Describe the morphology of the red blood cells.
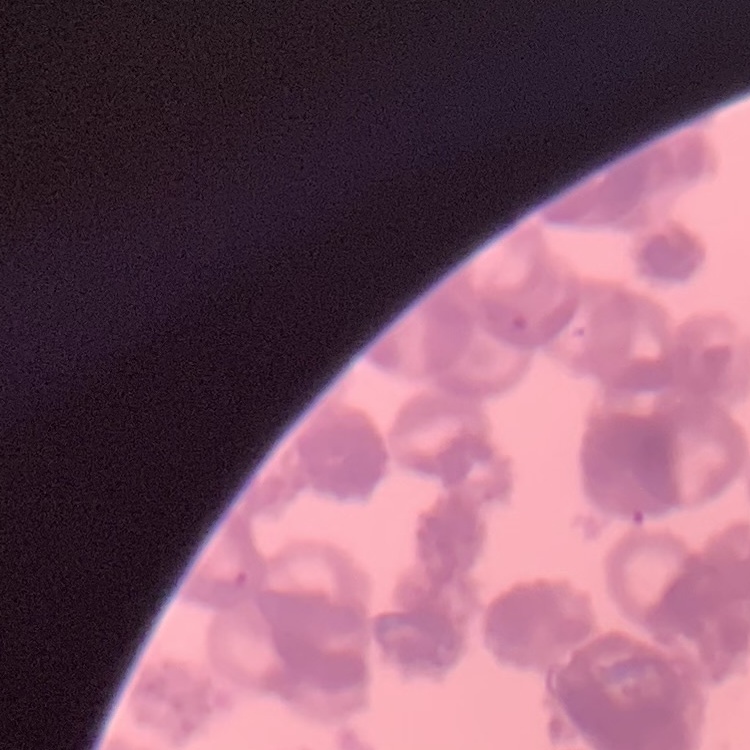

They show rouleaux formation.

Stained with either Field's or Giemsa. Square crop of a larger photomicrograph. Thin peripheral smear.